Point out each Plasmodium parasite.
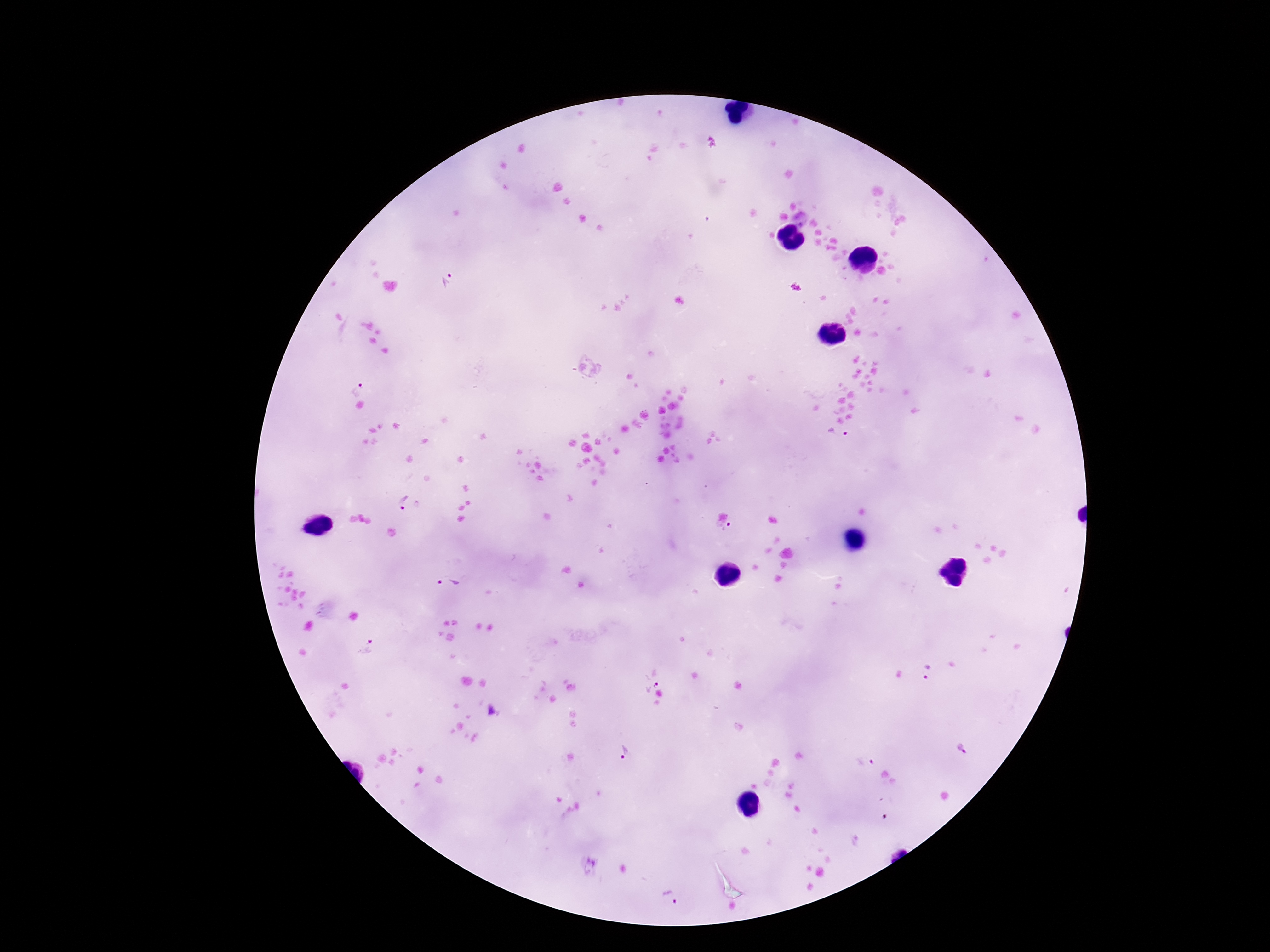

Approximate centers as (x, y) in pixels.
Plasmodium parasites: (444, 279), (358, 388), (838, 435), (401, 500), (724, 529), (449, 582), (367, 649), (928, 674), (648, 678), (493, 712), (962, 748), (624, 750), (865, 760), (587, 865), (669, 898).

{
  "magnification": "100x",
  "preparation": "thick peripheral-blood smear",
  "stain": "Giemsa",
  "field_of_view": "one from this slide",
  "capture": "smartphone camera through the microscope eyepiece",
  "image_size": "1270×952 pixels",
  "patient_malaria_status": "infected"
}